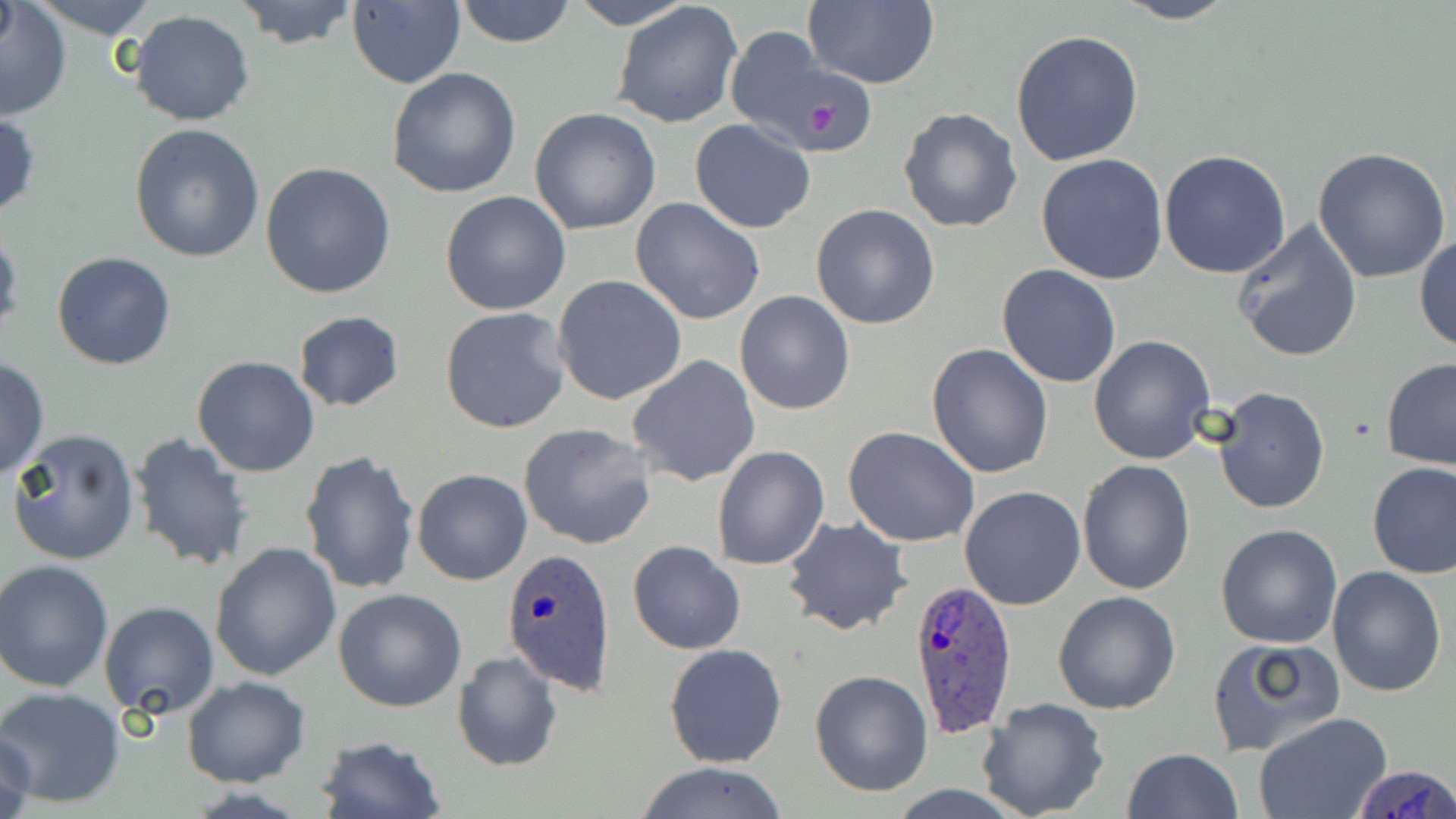

slide-level diagnosis = Plasmodium ovale
stain = May-Grünwald-Giemsa
field of view = single
magnification = 1000x
uninfected red blood cell locations = approximate bounding boxes as named x1/y1/x2/y2 corners in pixels: (x1=23, y1=0, x2=165, y2=38), (x1=235, y1=0, x2=358, y2=50), (x1=453, y1=0, x2=576, y2=49), (x1=566, y1=0, x2=698, y2=30), (x1=801, y1=0, x2=939, y2=90), (x1=1108, y1=0, x2=1241, y2=24), (x1=347, y1=1, x2=465, y2=88), (x1=612, y1=1, x2=744, y2=130), (x1=1, y1=3, x2=72, y2=121), (x1=128, y1=11, x2=257, y2=126), (x1=724, y1=28, x2=861, y2=153), (x1=1010, y1=29, x2=1144, y2=167), (x1=388, y1=67, x2=521, y2=198), (x1=898, y1=107, x2=1023, y2=232), (x1=530, y1=108, x2=660, y2=234), (x1=0, y1=111, x2=41, y2=220), (x1=690, y1=120, x2=817, y2=234), (x1=130, y1=125, x2=265, y2=263), (x1=1313, y1=148, x2=1452, y2=285), (x1=1158, y1=151, x2=1291, y2=278), (x1=1036, y1=153, x2=1169, y2=284), (x1=261, y1=162, x2=397, y2=299), (x1=440, y1=191, x2=571, y2=316), (x1=630, y1=196, x2=766, y2=325), (x1=811, y1=204, x2=941, y2=330), (x1=1231, y1=219, x2=1366, y2=362), (x1=0, y1=229, x2=23, y2=339), (x1=1414, y1=233, x2=1456, y2=354), (x1=52, y1=252, x2=177, y2=370), (x1=997, y1=264, x2=1123, y2=388), (x1=553, y1=275, x2=688, y2=407), (x1=735, y1=291, x2=855, y2=414), (x1=439, y1=306, x2=571, y2=434), (x1=293, y1=309, x2=404, y2=412), (x1=1088, y1=334, x2=1216, y2=465), (x1=927, y1=344, x2=1054, y2=480), (x1=192, y1=355, x2=321, y2=476), (x1=627, y1=355, x2=762, y2=487), (x1=0, y1=357, x2=48, y2=480), (x1=1382, y1=358, x2=1456, y2=471), (x1=1211, y1=385, x2=1329, y2=514), (x1=519, y1=423, x2=659, y2=550), (x1=843, y1=426, x2=980, y2=547), (x1=8, y1=428, x2=140, y2=566), (x1=131, y1=433, x2=254, y2=571), (x1=712, y1=447, x2=830, y2=571), (x1=299, y1=451, x2=421, y2=596), (x1=1077, y1=460, x2=1196, y2=595), (x1=1366, y1=462, x2=1456, y2=579), (x1=412, y1=469, x2=532, y2=586), (x1=959, y1=485, x2=1087, y2=611), (x1=782, y1=518, x2=911, y2=636), (x1=1215, y1=524, x2=1344, y2=649), (x1=637, y1=531, x2=758, y2=753), (x1=627, y1=539, x2=746, y2=654), (x1=210, y1=542, x2=341, y2=681), (x1=0, y1=560, x2=114, y2=692), (x1=1327, y1=566, x2=1447, y2=698), (x1=334, y1=588, x2=467, y2=712), (x1=1052, y1=591, x2=1180, y2=715), (x1=99, y1=601, x2=218, y2=718), (x1=1208, y1=636, x2=1344, y2=756), (x1=663, y1=643, x2=788, y2=769), (x1=452, y1=652, x2=561, y2=771), (x1=808, y1=670, x2=933, y2=797), (x1=182, y1=677, x2=309, y2=787), (x1=1, y1=687, x2=126, y2=808), (x1=977, y1=697, x2=1110, y2=819), (x1=1255, y1=714, x2=1393, y2=819), (x1=1, y1=729, x2=38, y2=819), (x1=315, y1=735, x2=445, y2=819), (x1=1122, y1=748, x2=1242, y2=819), (x1=632, y1=762, x2=792, y2=819)
preparation = thin blood film
platelet locations = approximate bounding boxes as named x1/y1/x2/y2 corners in pixels: (x1=806, y1=103, x2=841, y2=133)
Plasmodium ovale-infected red blood cell locations = approximate bounding boxes as named x1/y1/x2/y2 corners in pixels: (x1=502, y1=546, x2=618, y2=694), (x1=908, y1=578, x2=1021, y2=735), (x1=1350, y1=762, x2=1455, y2=818)
image size = 1456×819 pixels
modality = light microscopy